Give the extent of all Plasmodium malariae-infected red blood cells.
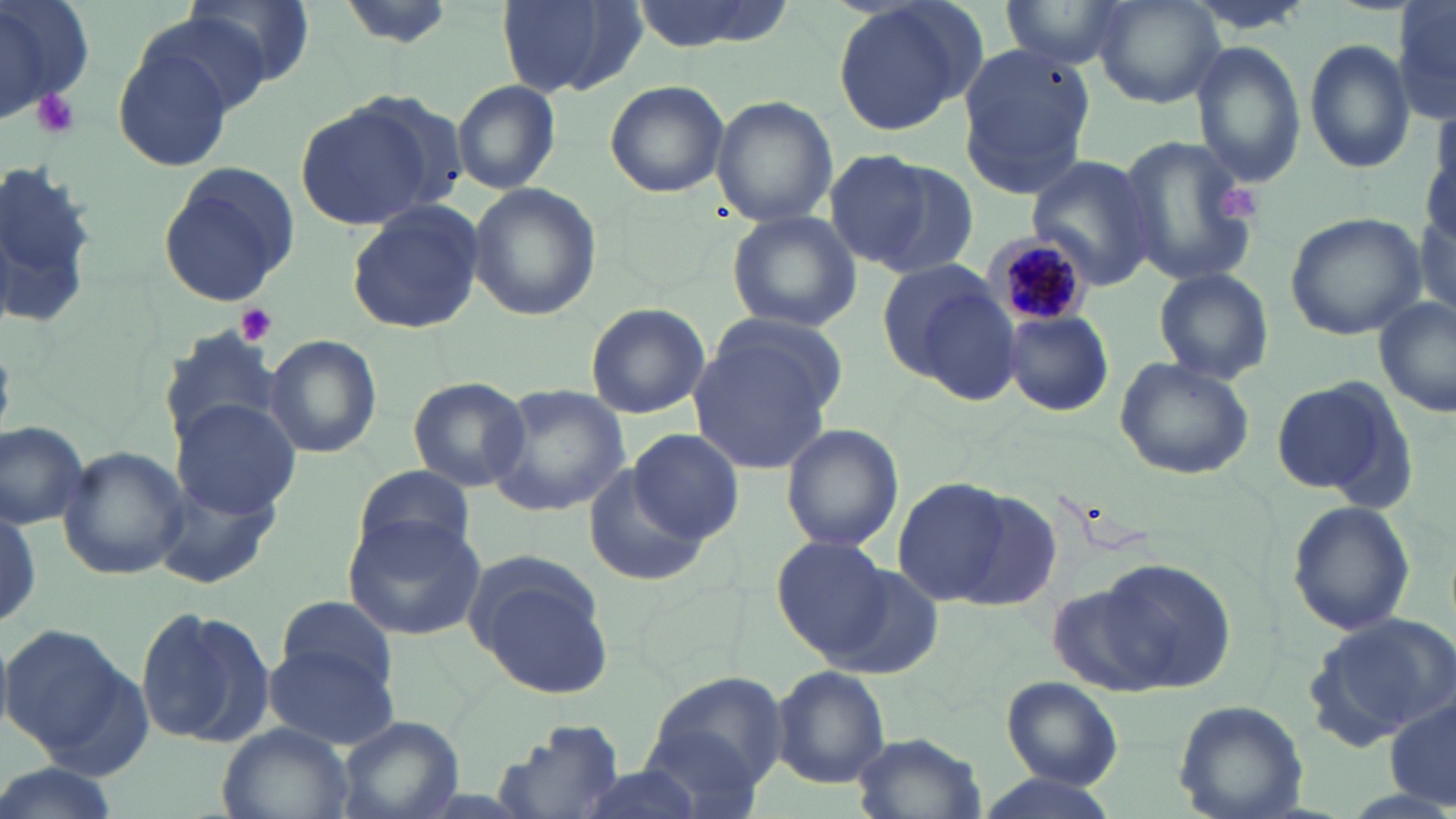
Approximate bounding boxes as (x1,y1)-(x2,y2) corner pairs in pixels.
Plasmodium malariae-infected red blood cells: (989,233)-(1090,330).

Platelet locations: (34,89)-(80,140), (1218,183)-(1265,228), (238,303)-(279,344). Uninfected red blood cell locations: (0,0)-(95,125), (178,0)-(313,96), (336,0)-(457,49), (497,0)-(644,99), (625,0)-(799,52), (828,0)-(985,140), (1004,0)-(1134,70), (1091,1)-(1225,108), (1392,1)-(1456,127), (131,7)-(276,124), (112,33)-(236,170), (1303,39)-(1416,175), (955,41)-(1095,200), (1191,42)-(1307,188), (604,80)-(729,198), (452,81)-(561,195), (712,98)-(836,225), (294,101)-(438,229), (1116,132)-(1265,293), (826,151)-(975,279), (1,154)-(100,334), (1026,154)-(1163,291), (157,162)-(302,306), (468,182)-(600,323), (347,200)-(485,334), (726,211)-(862,333), (1285,211)-(1426,339), (883,261)-(1023,399), (1152,268)-(1275,386), (1375,296)-(1455,417), (585,302)-(709,418), (1003,311)-(1113,417), (687,320)-(841,475), (158,323)-(287,447), (264,334)-(381,459), (1113,356)-(1255,480), (407,376)-(530,492), (1269,376)-(1406,500), (485,384)-(631,517), (171,398)-(301,519), (1,420)-(90,529), (782,424)-(904,552), (630,429)-(742,543), (57,447)-(189,580), (585,464)-(711,586), (352,465)-(477,569), (150,470)-(280,587), (892,478)-(1019,607), (1285,498)-(1417,637), (341,514)-(485,642), (773,537)-(893,660), (461,550)-(617,700), (1074,560)-(1240,694), (816,563)-(947,680), (275,594)-(402,695), (135,603)-(273,750), (1308,612)-(1456,746), (0,621)-(134,763), (262,639)-(399,749), (771,665)-(888,788), (646,671)-(789,791), (1001,676)-(1122,789), (1172,699)-(1308,819), (1386,699)-(1456,812), (335,715)-(463,819), (492,715)-(626,819), (214,721)-(354,819), (638,725)-(765,817), (850,732)-(985,819), (0,762)-(121,819), (559,765)-(714,819), (975,773)-(1120,819). Slide-level diagnosis: Plasmodium malariae. Thin blood smear. Optical microscopy. Image is 1456×819 pixels. May-Grünwald-Giemsa stain. Captured at 1000x magnification. Single field of view.